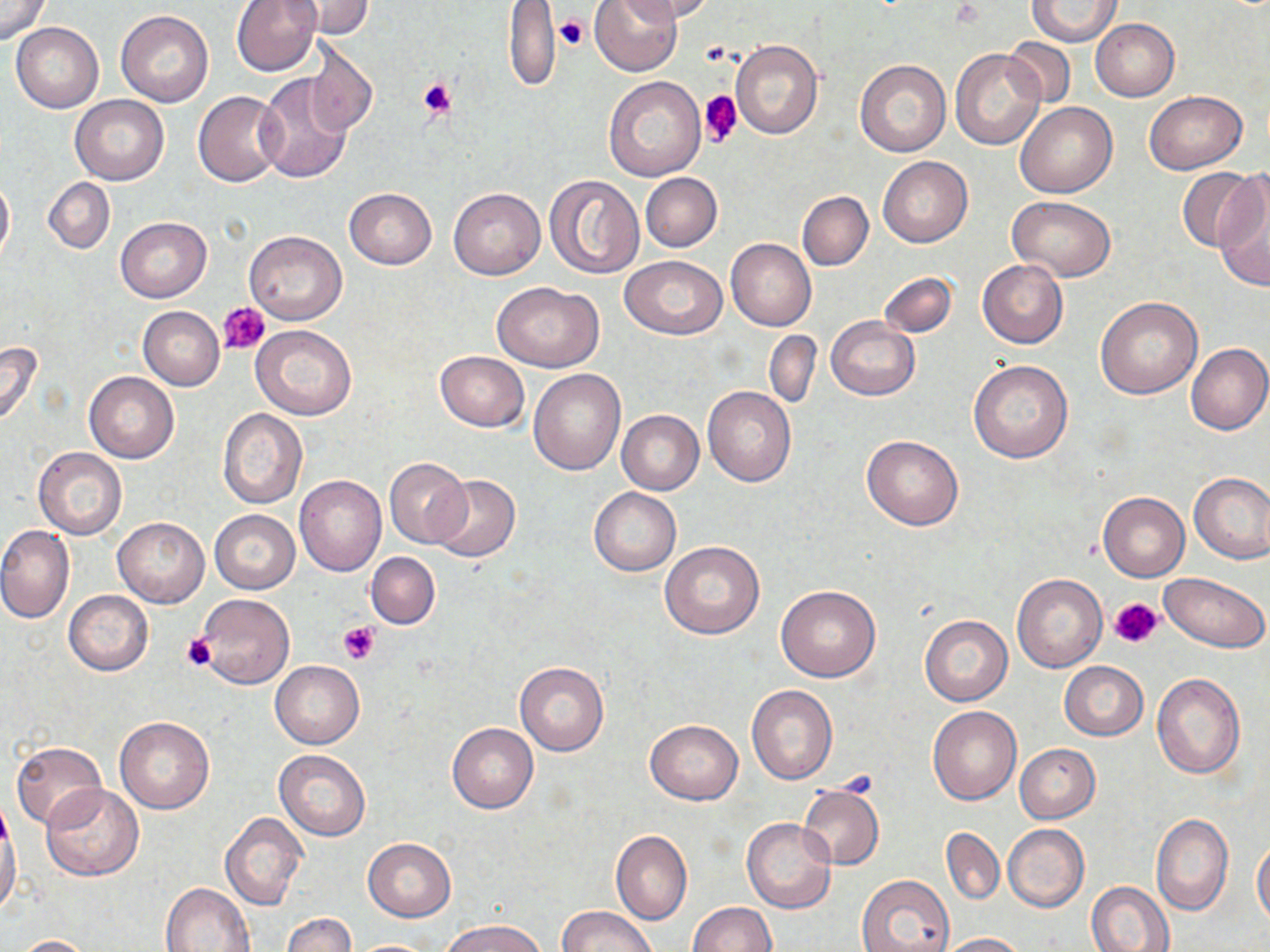 Approximate bounding boxes as (x1,y1)-(x2,y2) corner pairs in pixels. Platelet locations: (555,13)-(589,52), (417,77)-(456,119), (699,90)-(742,147), (218,302)-(270,355), (1110,597)-(1165,650), (339,622)-(380,663), (181,634)-(220,672). Uninfected red blood cell locations: (0,0)-(52,45), (231,0)-(320,76), (285,0)-(372,39), (589,0)-(681,75), (633,0)-(716,22), (1027,0)-(1121,46), (502,1)-(560,91), (116,10)-(214,106), (1090,18)-(1180,100), (12,22)-(104,113), (304,38)-(377,139), (1005,38)-(1076,108), (731,41)-(824,139), (950,49)-(1045,150), (854,59)-(949,157), (255,75)-(352,183), (605,76)-(706,181), (192,90)-(288,188), (1144,90)-(1247,174), (70,95)-(169,185), (1015,103)-(1117,198), (878,156)-(972,247), (1178,167)-(1260,253), (641,173)-(722,252), (1213,174)-(1270,290), (0,175)-(13,264), (545,175)-(644,279), (44,178)-(115,254), (344,187)-(437,268), (449,187)-(545,279), (798,190)-(874,271), (1008,196)-(1115,281), (115,216)-(212,303), (243,230)-(346,325), (726,238)-(816,331), (620,256)-(727,338), (977,260)-(1068,348), (878,271)-(957,339), (493,281)-(603,372), (1095,297)-(1203,399), (137,306)-(224,390), (827,315)-(920,400), (251,325)-(359,420), (764,330)-(821,410), (0,341)-(43,429), (1186,342)-(1269,435), (435,350)-(528,431), (969,359)-(1074,462), (528,368)-(625,475), (84,371)-(179,463), (703,386)-(796,486), (217,408)-(308,508), (617,409)-(704,494), (861,433)-(964,531), (34,447)-(126,538), (385,457)-(472,548), (1188,471)-(1270,563), (429,474)-(521,562), (294,475)-(386,577), (589,487)-(681,576), (1098,492)-(1190,580), (211,509)-(299,594), (113,517)-(208,607), (0,526)-(74,625), (659,541)-(764,639), (366,552)-(439,629), (1160,572)-(1268,653), (1011,574)-(1107,671), (775,585)-(881,682), (63,591)-(153,675), (195,594)-(294,690), (919,615)-(1013,706), (270,660)-(364,749), (514,661)-(609,756), (1059,661)-(1149,741), (1152,674)-(1246,778), (746,685)-(838,784), (927,706)-(1023,805), (115,717)-(214,814), (644,719)-(744,805), (447,723)-(538,813), (11,741)-(107,830), (1015,744)-(1100,823), (274,749)-(370,841), (40,784)-(144,881), (798,784)-(884,869), (0,813)-(22,921), (220,813)-(306,911), (1151,813)-(1233,916), (741,817)-(836,915), (1003,824)-(1089,913), (611,829)-(691,925), (941,829)-(1005,904), (363,838)-(455,922), (1253,840)-(1270,926), (857,874)-(956,952), (1087,881)-(1176,952), (161,882)-(256,951), (687,902)-(776,952), (558,906)-(656,952), (281,913)-(355,952), (445,919)-(545,952), (936,932)-(1026,951), (12,935)-(99,952), (348,939)-(441,951). Slide-level diagnosis: negative for blood parasites. One field of a larger specimen. Light microscopy. Thin blood film. May-Grünwald-Giemsa-stained preparation. 1000x magnification. Image is 1270×952 pixels.